State the blood parasite species.
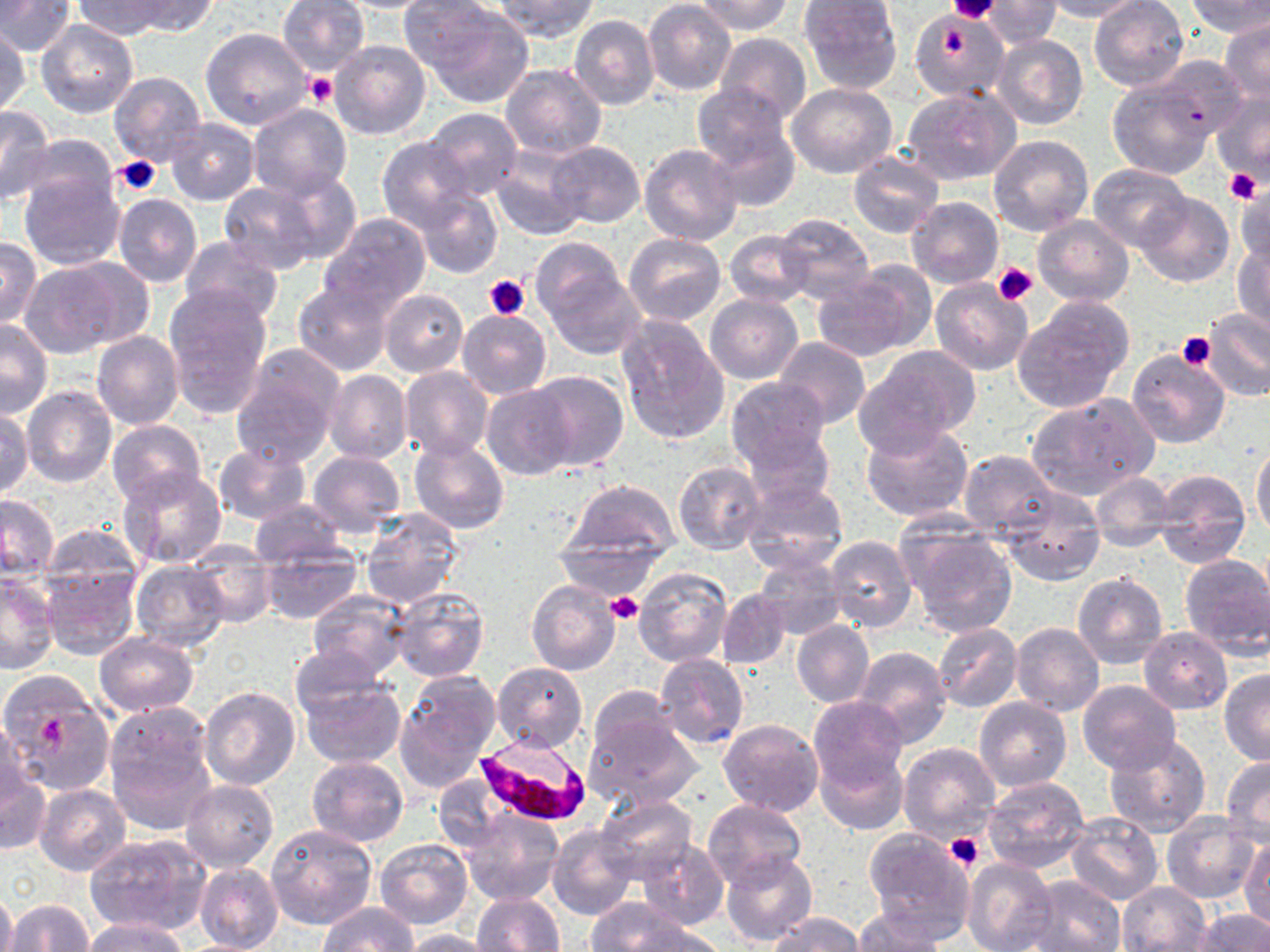
Plasmodium falciparum.

Approximate bounding boxes as (x1, y1, x2, y2) in pixels. Uninfected red blood cell locations: (71, 0, 168, 40), (121, 0, 219, 36), (278, 0, 369, 76), (493, 0, 600, 42), (694, 0, 793, 35), (799, 0, 903, 93), (984, 0, 1059, 45), (1038, 0, 1144, 22), (1088, 0, 1190, 91), (1184, 0, 1270, 36), (0, 1, 75, 56), (331, 1, 445, 12), (644, 1, 736, 97), (415, 3, 535, 108), (908, 7, 1009, 102), (569, 14, 659, 111), (37, 20, 139, 119), (1219, 20, 1270, 103), (201, 27, 311, 131), (1, 29, 31, 116), (715, 33, 812, 124), (993, 34, 1088, 131), (328, 40, 430, 141), (1154, 56, 1246, 138), (498, 65, 607, 160), (108, 71, 206, 169), (1107, 78, 1213, 179), (788, 83, 898, 178), (693, 86, 800, 201), (903, 86, 1019, 186), (1212, 91, 1270, 184), (248, 105, 352, 199), (0, 106, 54, 205), (422, 107, 522, 200), (164, 118, 259, 206), (16, 134, 118, 214), (988, 134, 1093, 236), (376, 136, 476, 231), (548, 141, 645, 227), (640, 144, 744, 247), (490, 148, 586, 241), (847, 150, 944, 239), (1087, 165, 1193, 251), (265, 168, 363, 266), (19, 171, 125, 270), (216, 181, 321, 274), (1232, 183, 1270, 271), (414, 189, 502, 280), (1133, 192, 1234, 287), (112, 195, 201, 287), (908, 197, 1003, 289), (320, 212, 431, 315), (776, 212, 875, 305), (1032, 216, 1134, 308), (725, 231, 814, 309), (624, 232, 725, 325), (0, 235, 42, 329), (179, 236, 284, 325), (1233, 239, 1270, 336), (535, 247, 642, 359), (59, 256, 157, 350), (19, 261, 127, 357), (854, 261, 936, 349), (809, 274, 919, 362), (929, 279, 1033, 375), (294, 281, 395, 375), (161, 286, 272, 422), (380, 289, 468, 377), (705, 294, 802, 383), (1013, 298, 1133, 413), (457, 309, 551, 398), (1200, 309, 1270, 400), (617, 316, 729, 445), (0, 319, 53, 418), (91, 330, 183, 430), (773, 338, 872, 430), (859, 345, 982, 450), (232, 348, 344, 464), (1128, 350, 1230, 449), (400, 366, 494, 462), (325, 369, 413, 463), (529, 369, 629, 471), (724, 376, 831, 470), (483, 384, 576, 480), (22, 386, 116, 487), (1025, 394, 1158, 501), (1, 408, 33, 498), (105, 419, 206, 508), (860, 423, 972, 523), (741, 427, 836, 507), (409, 437, 508, 533), (1251, 441, 1270, 541), (212, 442, 312, 526), (959, 450, 1058, 541), (309, 452, 404, 537), (673, 461, 767, 555), (118, 467, 226, 569), (1154, 468, 1251, 569), (1090, 472, 1178, 549), (562, 479, 681, 565), (740, 479, 848, 575), (999, 486, 1105, 585), (0, 495, 60, 581), (249, 500, 348, 570), (359, 509, 463, 609), (897, 521, 1017, 637), (39, 523, 145, 608), (824, 536, 915, 632), (184, 545, 277, 626), (257, 546, 362, 624), (1181, 554, 1270, 658), (755, 555, 848, 641), (131, 560, 229, 650), (41, 564, 139, 660), (634, 566, 733, 667), (0, 574, 59, 673), (1073, 574, 1166, 669), (527, 580, 621, 676), (389, 585, 489, 682), (718, 588, 792, 670), (307, 590, 411, 680), (792, 620, 874, 708), (1011, 623, 1104, 718), (932, 624, 1022, 713), (1139, 628, 1232, 714), (94, 633, 200, 716), (852, 646, 952, 747), (290, 649, 388, 730), (655, 654, 750, 750), (492, 662, 588, 754), (394, 670, 499, 790), (1219, 670, 1270, 766), (0, 672, 114, 794), (298, 679, 405, 769), (1077, 680, 1182, 775), (199, 686, 300, 790), (19, 696, 111, 790), (973, 696, 1070, 791), (808, 697, 908, 794), (579, 699, 703, 812), (105, 706, 215, 826), (0, 716, 25, 817), (718, 719, 823, 816), (1103, 732, 1211, 838), (896, 742, 1000, 845), (817, 747, 906, 835), (1220, 754, 1270, 848), (307, 755, 408, 846), (0, 767, 51, 854), (983, 776, 1090, 874), (182, 781, 278, 873), (35, 784, 131, 876), (595, 796, 696, 884), (703, 800, 807, 890), (460, 809, 562, 905), (1065, 813, 1163, 905), (1160, 815, 1262, 904), (265, 824, 377, 931), (548, 825, 637, 921), (864, 827, 977, 940), (84, 832, 210, 934), (636, 836, 729, 931), (374, 837, 472, 930), (1239, 838, 1269, 930), (722, 851, 816, 946), (962, 858, 1056, 952), (196, 862, 284, 952), (1022, 874, 1126, 952), (1117, 881, 1211, 951), (0, 890, 16, 952), (473, 892, 564, 952), (5, 899, 92, 951), (587, 899, 693, 950), (317, 903, 418, 952), (851, 907, 948, 951), (1192, 909, 1270, 952), (770, 913, 863, 952), (81, 918, 191, 951), (622, 925, 730, 952), (398, 929, 502, 951). Plasmodium falciparum-infected red blood cell locations: (473, 727, 586, 825). Platelet locations: (948, 1, 1001, 24), (304, 74, 337, 107), (114, 154, 163, 195), (1225, 169, 1262, 203), (993, 262, 1038, 305), (483, 275, 530, 319), (1176, 331, 1216, 371), (605, 591, 643, 626), (42, 716, 67, 747), (944, 833, 983, 872). Thin blood film. Image is 1270×952 pixels. Optical microscopy. Single field of view. Captured at 1000x magnification. May-Grünwald-Giemsa-stained preparation.